Report the malaria status.
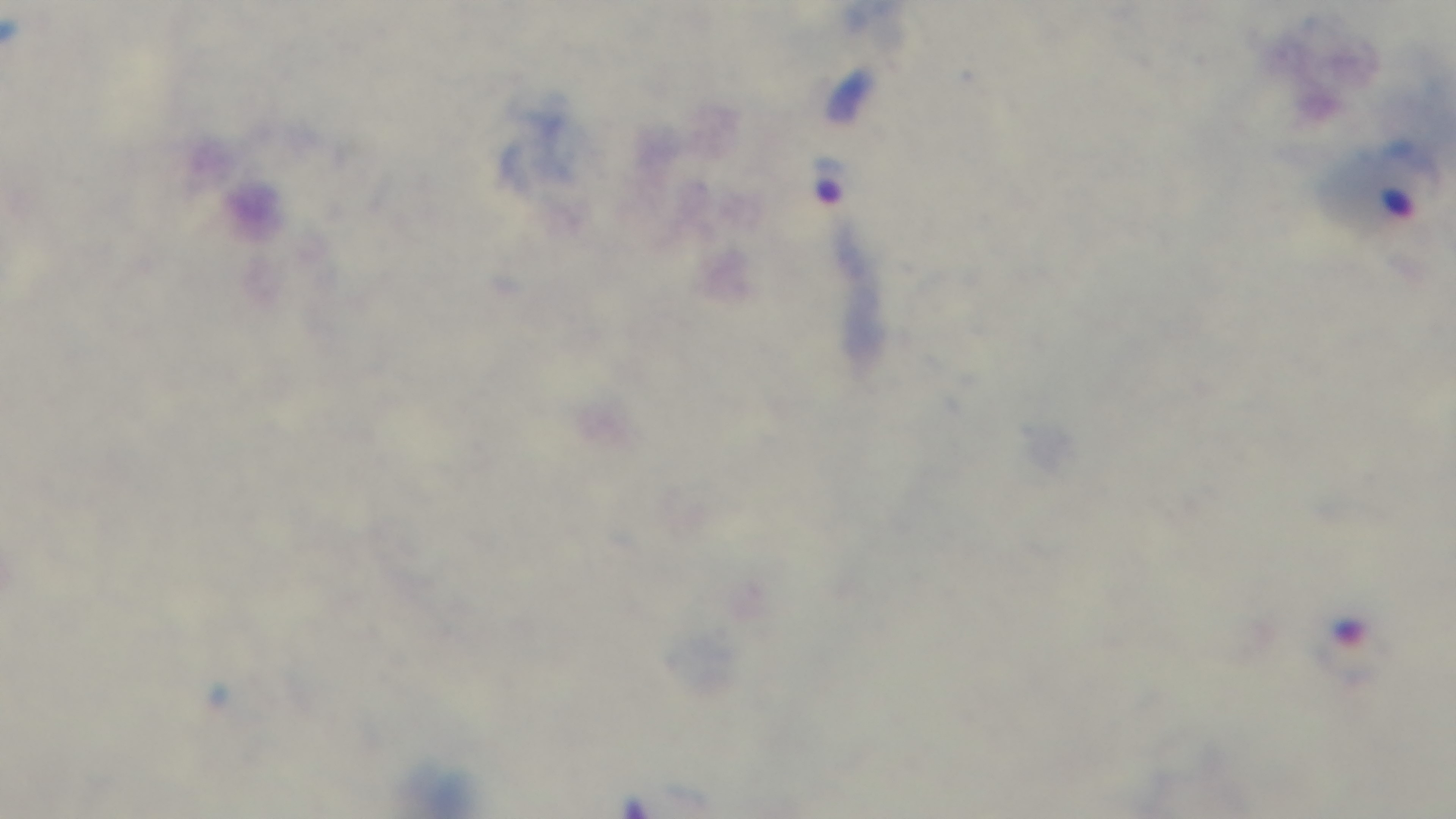
It is infected.

capture: mounted 4K digital camera
objective: 100x oil immersion
field_of_view: single
stain: Giemsa
preparation: thick
modality: light microscopy